Assess this cell for malaria.
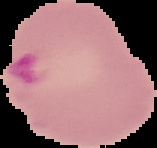

It is parasitized.

Cell region segmented out of the field of view; the surrounding area is masked to black. From a thin blood smear. Image is 157×148 pixels.